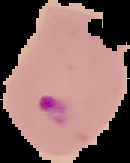
Cell region segmented out of the field of view; the surrounding area is masked to black. Result: malaria parasites identified. Image is 130×163 pixels. From a thin blood smear.